Comment on the morphology of the erythrocytes.
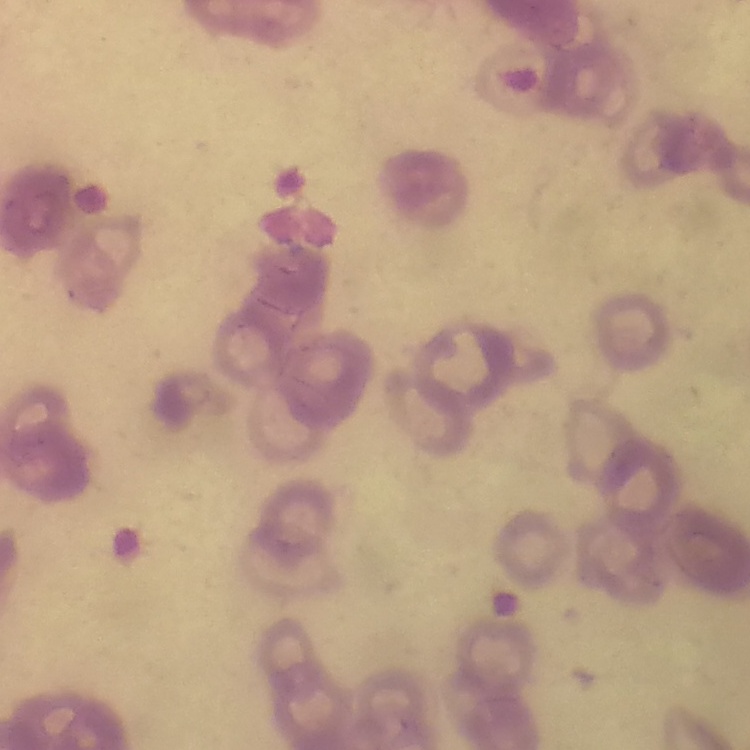
Rouleaux formation.

preparation: thin peripheral smear
stain: Field's or Giemsa
image_type: one tile cut from a larger photomicrograph